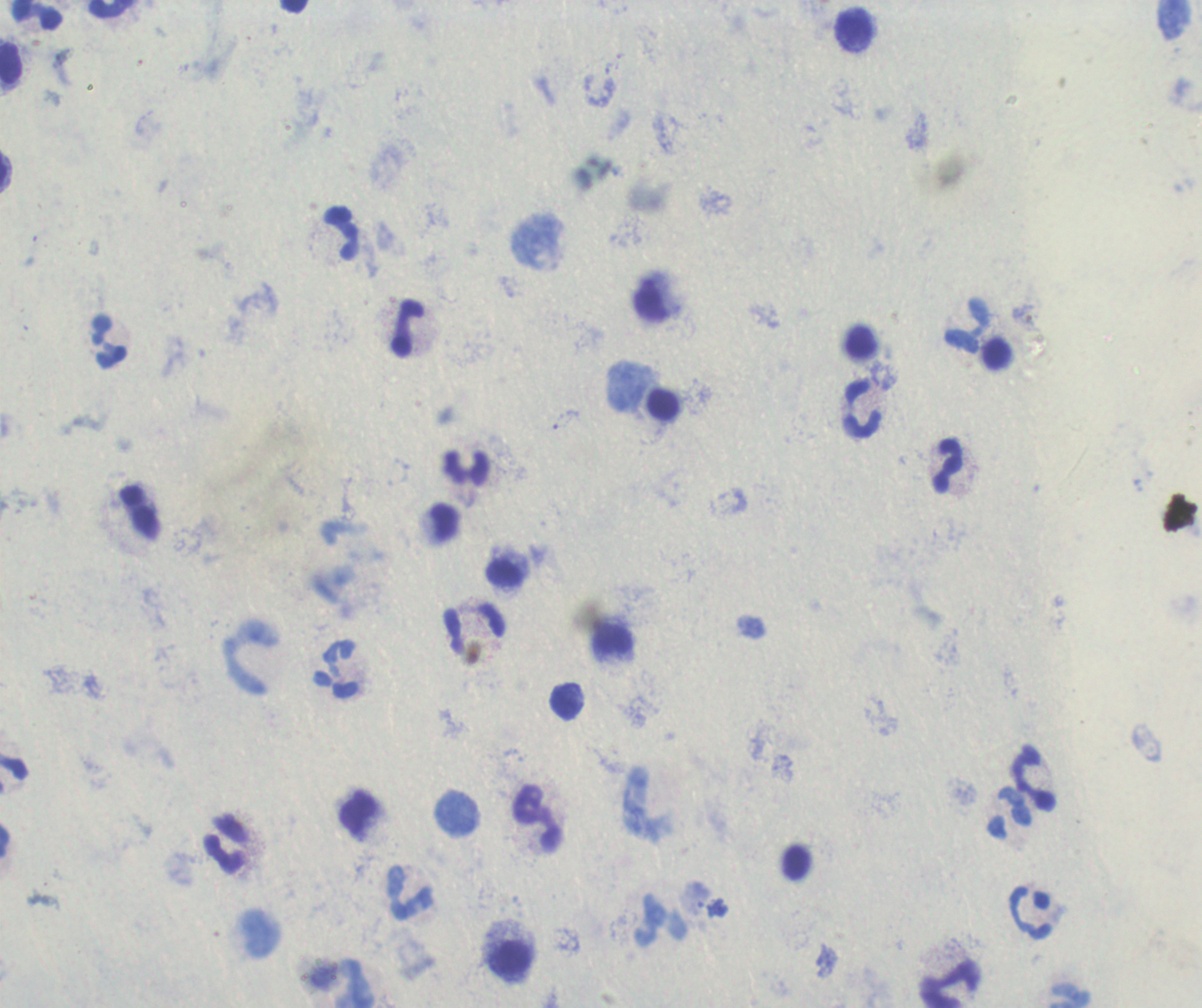
Approximate centers as (x, y) in pixels.
Summary:
  - Leukocyte locations: (111, 9), (37, 15), (854, 29), (11, 63), (342, 233), (651, 299), (969, 325), (408, 329), (109, 341), (664, 406), (862, 409), (948, 466), (468, 467), (444, 522), (504, 572), (473, 628), (613, 641), (250, 658), (337, 670), (566, 702), (13, 775), (1035, 779), (644, 804), (358, 813), (457, 813), (1009, 813), (537, 819), (225, 843), (411, 892), (1029, 913), (660, 921), (510, 959), (950, 984)
  - Image size: 1202×1008 pixels
  - Result: negative for Plasmodium parasites
  - Background quality: unsatisfactory
  - Context: previously used in a real diagnosis
  - Field of view: one from this slide
  - Magnification: 100x
  - Stain: Romanowsky
  - Preparation: thick blood film